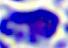

Captured at 400x magnification. A white blood cell is shown. Micrograph.